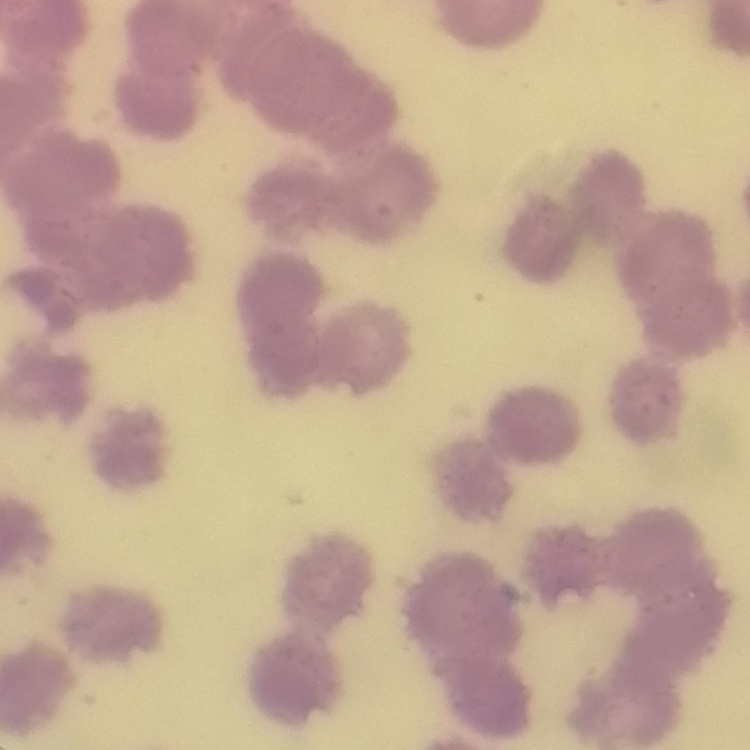
red blood cell morphology = rouleaux formation
stain = Field's or Giemsa
preparation = thin blood smear
image type = one tile cut from a larger photomicrograph